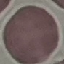
Summary:
  - Malaria status: uninfected
  - Image type: cell patch, automatically extracted from a larger field of view and resized to 64 × 64 pixels
  - Capture: smartphone through the microscope eyepiece
  - Stain: Giemsa
  - Preparation: thin blood smear